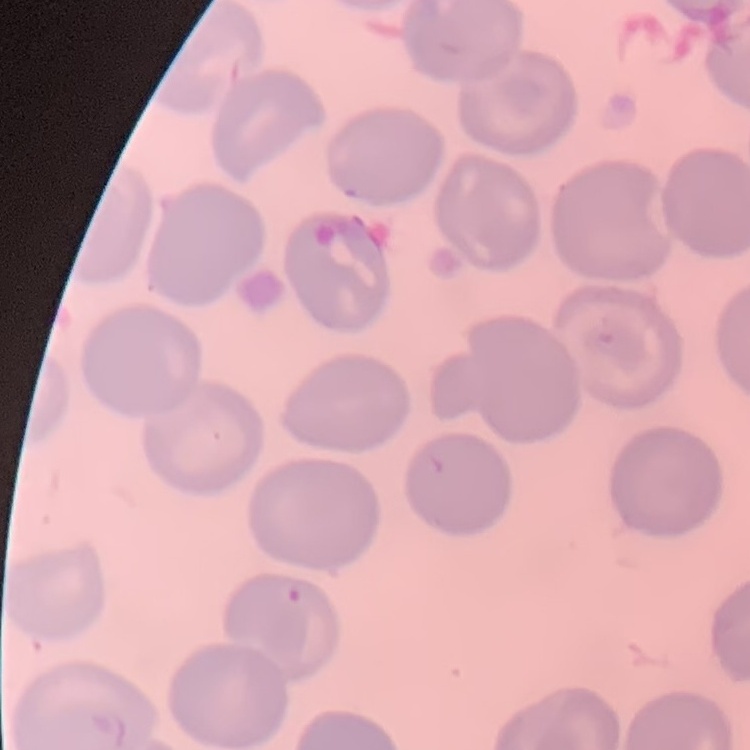
Summary:
  - Red blood cell morphology: no rouleaux formation
  - Preparation: thin blood smear
  - Stain: Field's or Giemsa
  - Image type: square crop of a larger photomicrograph